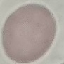
Summary:
  - Malaria status: uninfected
  - Preparation: thin blood film
  - Capture: smartphone through the microscope eyepiece
  - Stain: Giemsa
  - Image type: automatically extracted cell patch, resized to 64 × 64 pixels